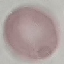
Malaria status: uninfected. Thin smear of blood. Giemsa stain. Acquired by smartphone through the microscope eyepiece. Cell patch, automatically extracted from a larger field of view and resized to 64 × 64 pixels.